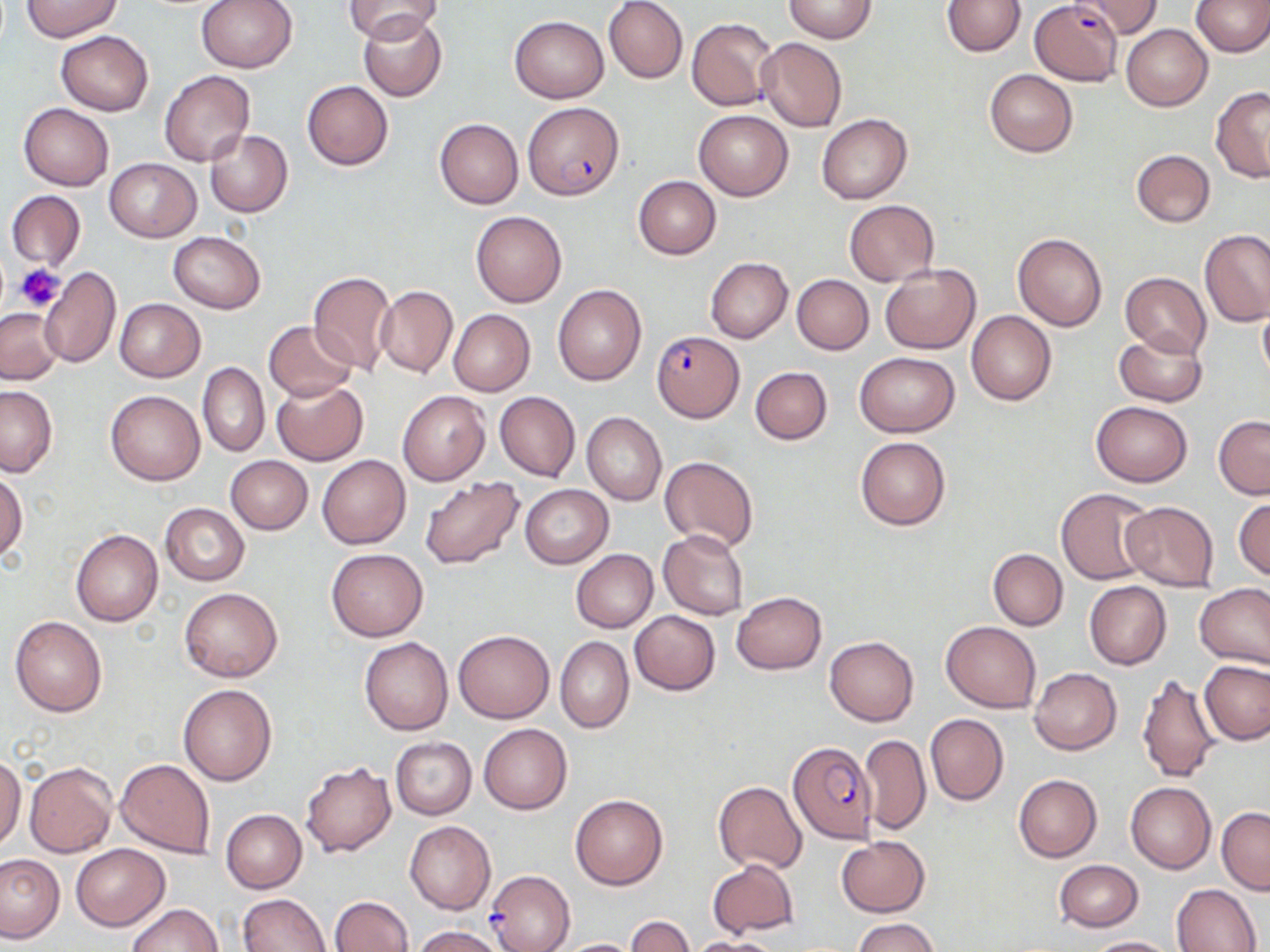
slide-level diagnosis = Plasmodium falciparum
platelet locations = approximate bounding boxes as (x1, y1, x2, y2) in pixels: (15, 264, 65, 310)
stain = May-Grünwald-Giemsa
uninfected red blood cell locations = approximate bounding boxes as (x1, y1, x2, y2) in pixels: (197, 0, 297, 72), (344, 0, 443, 44), (784, 0, 876, 43), (941, 0, 1025, 57), (1080, 0, 1163, 38), (1191, 0, 1270, 56), (21, 1, 122, 41), (603, 1, 688, 84), (358, 14, 447, 101), (510, 15, 609, 102), (686, 18, 777, 111), (1121, 24, 1212, 111), (55, 30, 154, 115), (755, 38, 847, 132), (985, 69, 1077, 156), (160, 70, 255, 167), (302, 80, 393, 169), (1211, 86, 1270, 182), (19, 104, 114, 190), (694, 110, 793, 200), (817, 113, 912, 203), (434, 119, 523, 208), (205, 129, 293, 217), (1131, 149, 1215, 227), (105, 158, 200, 241), (633, 176, 720, 259), (5, 190, 85, 273), (844, 200, 939, 286), (470, 209, 567, 307), (1199, 229, 1269, 326), (167, 232, 267, 313), (1012, 233, 1107, 330), (706, 257, 793, 343), (878, 263, 980, 354), (39, 267, 121, 367), (308, 269, 397, 374), (1119, 272, 1211, 358), (791, 274, 873, 354), (552, 285, 646, 386), (375, 286, 458, 377), (115, 299, 206, 382), (1257, 301, 1270, 387), (0, 308, 62, 383), (449, 309, 535, 395), (966, 310, 1058, 405), (263, 321, 358, 402), (1114, 331, 1207, 406), (855, 352, 959, 437), (197, 363, 268, 457), (750, 367, 832, 445), (272, 380, 368, 466), (0, 386, 57, 477), (105, 390, 204, 485), (398, 391, 491, 486), (495, 392, 580, 481), (1090, 400, 1192, 485), (582, 411, 667, 506), (1213, 416, 1270, 499), (856, 436, 951, 531), (316, 455, 411, 549), (225, 456, 313, 534), (659, 456, 759, 552), (0, 471, 26, 563), (418, 477, 524, 570), (521, 484, 612, 567), (1055, 488, 1155, 585), (1233, 498, 1270, 584), (1121, 501, 1220, 591), (160, 503, 249, 585), (70, 528, 163, 626), (658, 530, 750, 621), (325, 548, 428, 641), (988, 548, 1068, 630), (570, 549, 658, 633), (1084, 581, 1172, 669), (1196, 582, 1270, 671), (179, 588, 283, 682), (732, 591, 827, 675), (629, 611, 720, 694), (10, 616, 108, 717), (940, 621, 1041, 713), (453, 630, 554, 723), (825, 636, 919, 725), (360, 637, 454, 734), (556, 637, 634, 733), (1200, 660, 1270, 744), (1030, 668, 1122, 754), (1136, 669, 1225, 782), (178, 682, 278, 786), (925, 714, 1008, 805), (479, 723, 573, 814), (859, 733, 930, 835), (390, 736, 475, 819), (0, 755, 25, 852), (115, 758, 215, 857), (24, 761, 115, 857), (302, 761, 395, 858), (1014, 774, 1102, 862), (714, 782, 807, 872), (1125, 782, 1217, 874), (571, 794, 667, 889), (1217, 807, 1270, 894), (221, 809, 307, 892), (405, 821, 495, 914), (836, 837, 930, 916), (70, 843, 169, 929), (0, 854, 67, 944), (1054, 859, 1143, 932), (707, 860, 798, 937), (1172, 884, 1261, 951), (238, 893, 330, 952), (330, 896, 413, 952), (125, 903, 223, 952), (626, 916, 695, 952), (851, 917, 940, 952), (411, 925, 506, 952), (1083, 936, 1178, 952), (688, 937, 783, 952), (553, 938, 643, 951)
modality = light microscopy
preparation = thin blood film
Plasmodium falciparum-infected red blood cell locations = approximate bounding boxes as (x1, y1, x2, y2) in pixels: (1030, 1, 1122, 86), (523, 102, 624, 201), (652, 331, 744, 421), (788, 741, 876, 843), (486, 870, 575, 952)
field of view = one of a larger specimen
image size = 1270×952 pixels
magnification = 1000x